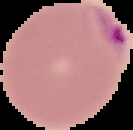

Summary:
  - Preparation: thin blood film
  - Result: malaria parasites identified
  - Image size: 133×130 pixels
  - Image type: cell region segmented out of the field of view; surrounding area masked to black